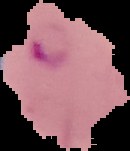
{
  "preparation": "thin blood smear",
  "malaria_status": "parasitized",
  "image_type": "segmented cell region with the area outside set to black",
  "image_size": "130×151 pixels"
}